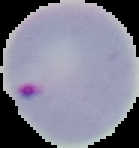
preparation = thin blood film
image size = 139×148 pixels
image type = segmented cell region with the area outside set to black
malaria status = parasitized